Locate every Plasmodium falciparum parasite and identify its life-cycle stage.
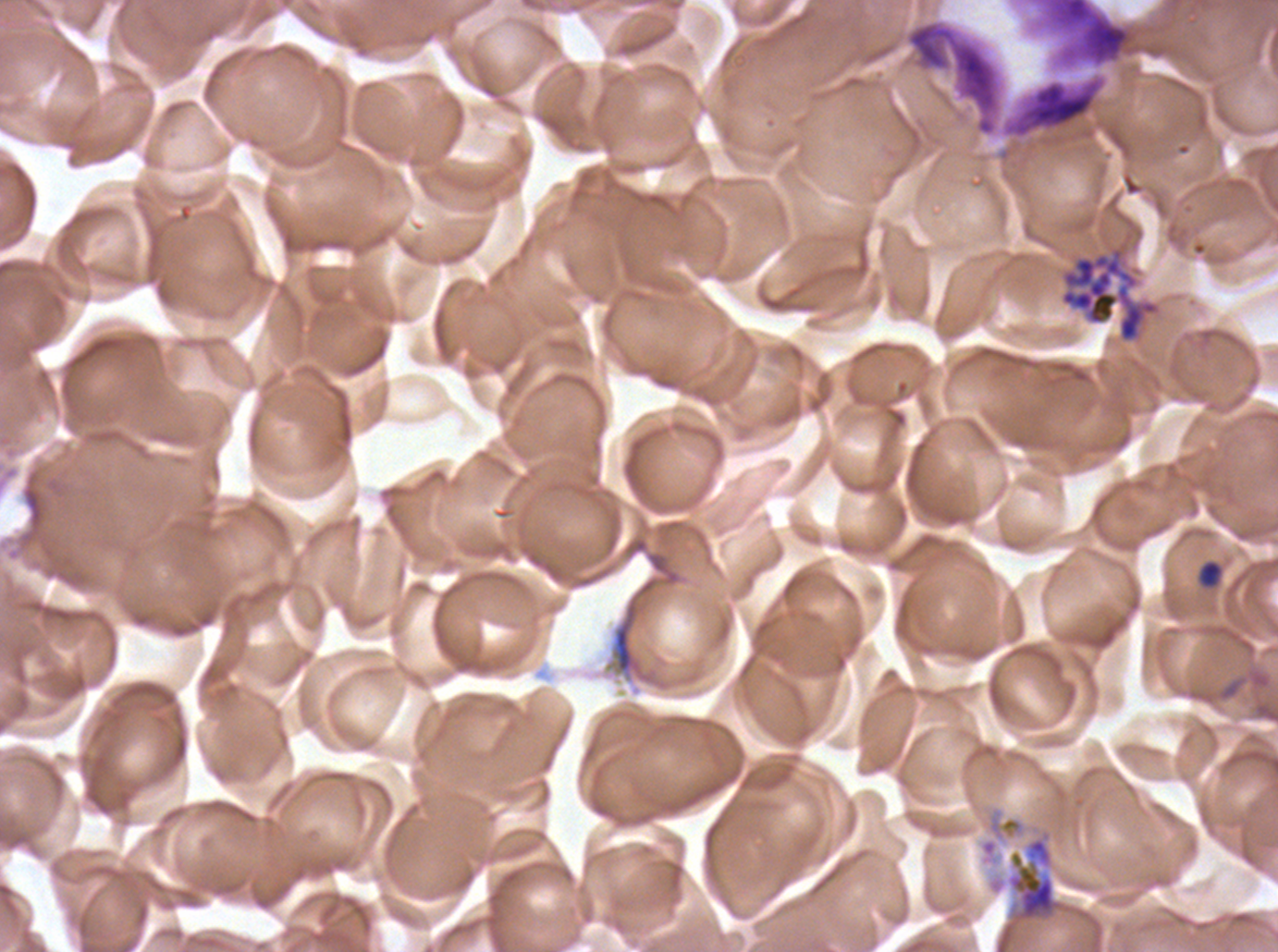
Approximate bounding boxes as [x1, y1, x2, y2] in pixels.
Late-ring/early-trophozoite forms: [1197, 558, 1224, 590].
Segmenters: [1059, 239, 1162, 344], [1006, 836, 1064, 923].
No rings, mid trophozoites, late trophozoites, early schizonts, late schizonts, or gametocytes observed.

Summary:
  - Debris locations: [903, 18, 1130, 140], [613, 601, 639, 674]
  - Life-cycle stages observed: late-ring/early-trophozoite, segmenter
  - Preparation: thin blood smear
  - Image size: 1278×952 pixels
  - Stain: Giemsa
  - Field of view: sub-image separated from a larger composite
  - Specimen: Plasmodium falciparum cultured ex vivo for 24 to 48 hours, from a patient in The Gambia